Report the malaria status of this cell.
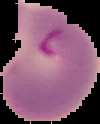

Parasitized.

{
  "preparation": "thin blood smear",
  "image_type": "cell region segmented out of the field of view; surrounding area masked to black",
  "image_size": "100×124 pixels"
}